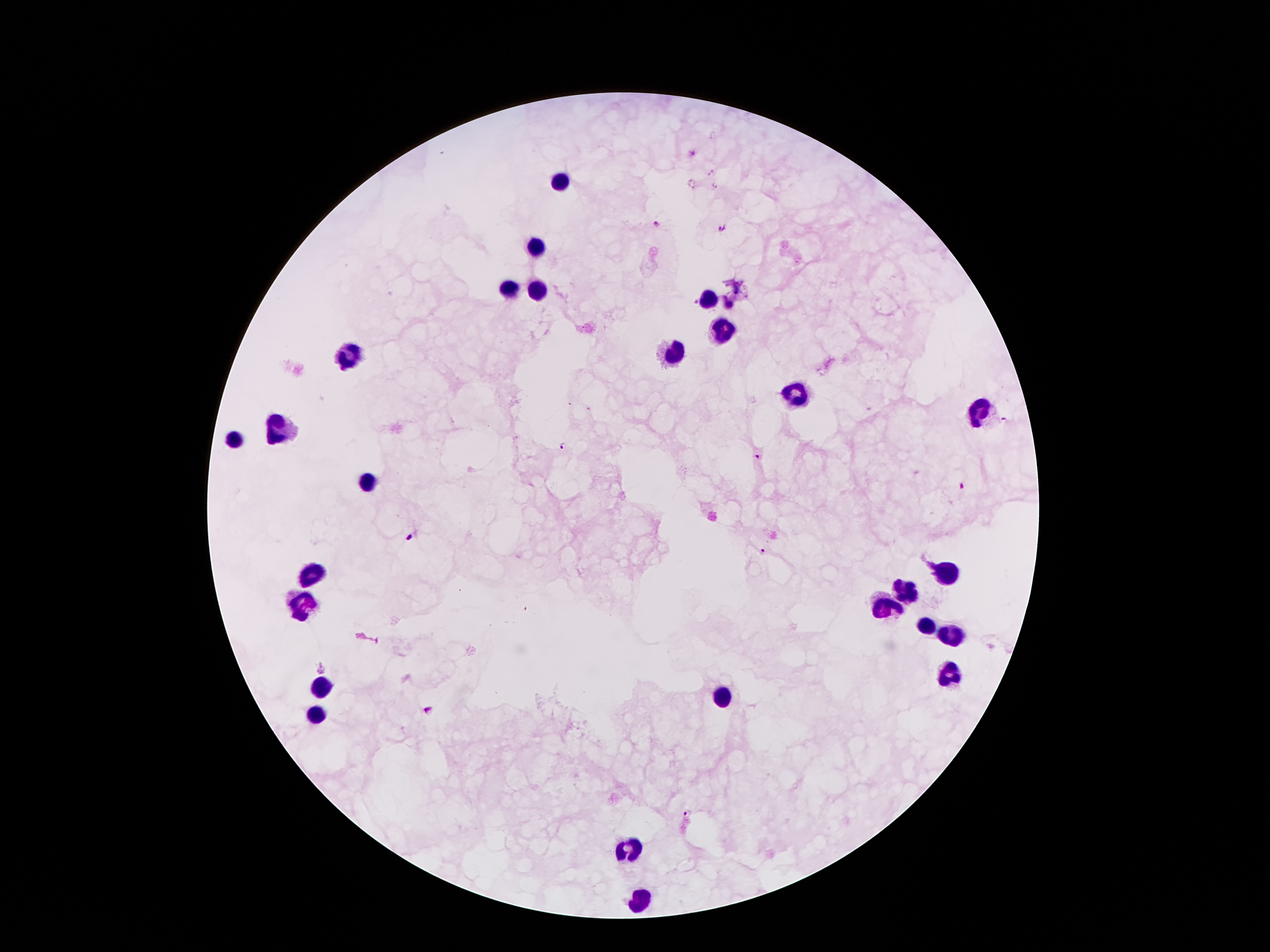 Approximate centers as (x, y) in pixels. Leukocyte locations: (555, 182), (533, 248), (535, 289), (506, 291), (707, 301), (723, 334), (348, 353), (676, 353), (795, 394), (979, 414), (281, 428), (232, 441), (369, 480), (943, 570), (313, 572), (902, 588), (883, 603), (301, 605), (926, 625), (951, 638), (949, 674), (322, 685), (723, 697), (314, 715), (631, 847), (643, 900). Plasmodium parasite locations: (691, 152), (709, 172), (691, 185), (713, 186), (657, 225), (721, 227), (1005, 420), (562, 447), (757, 456), (962, 485), (410, 538), (761, 551), (323, 667), (431, 709), (688, 813). Giemsa stain. 100x magnification. Patient malaria status: positive for Plasmodium falciparum. Photographed through the microscope eyepiece with a smartphone camera. Single field of view. Thick blood smear. Image is 1270×952 pixels.